Comment on the morphology of the erythrocytes.
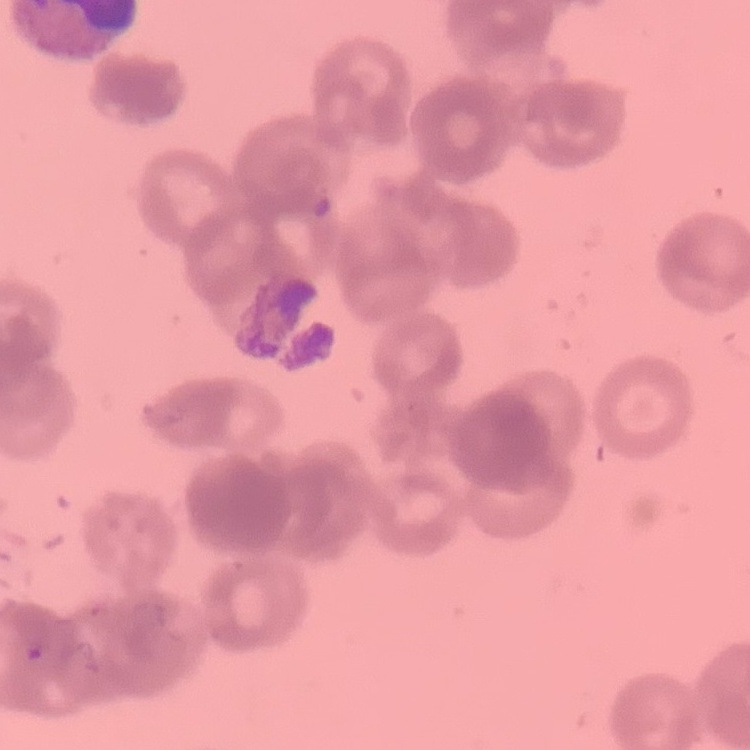
They show rouleaux formation.

Thin blood film. Field's or Giemsa stain. One tile cut from a larger photomicrograph.